Assess this cell for malaria.
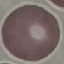

It is uninfected.

Cell patch, automatically extracted from a larger field of view and resized to 64 × 64 pixels. Thin smear of blood. Photographed with a smartphone camera at the microscope eyepiece. Giemsa stain.